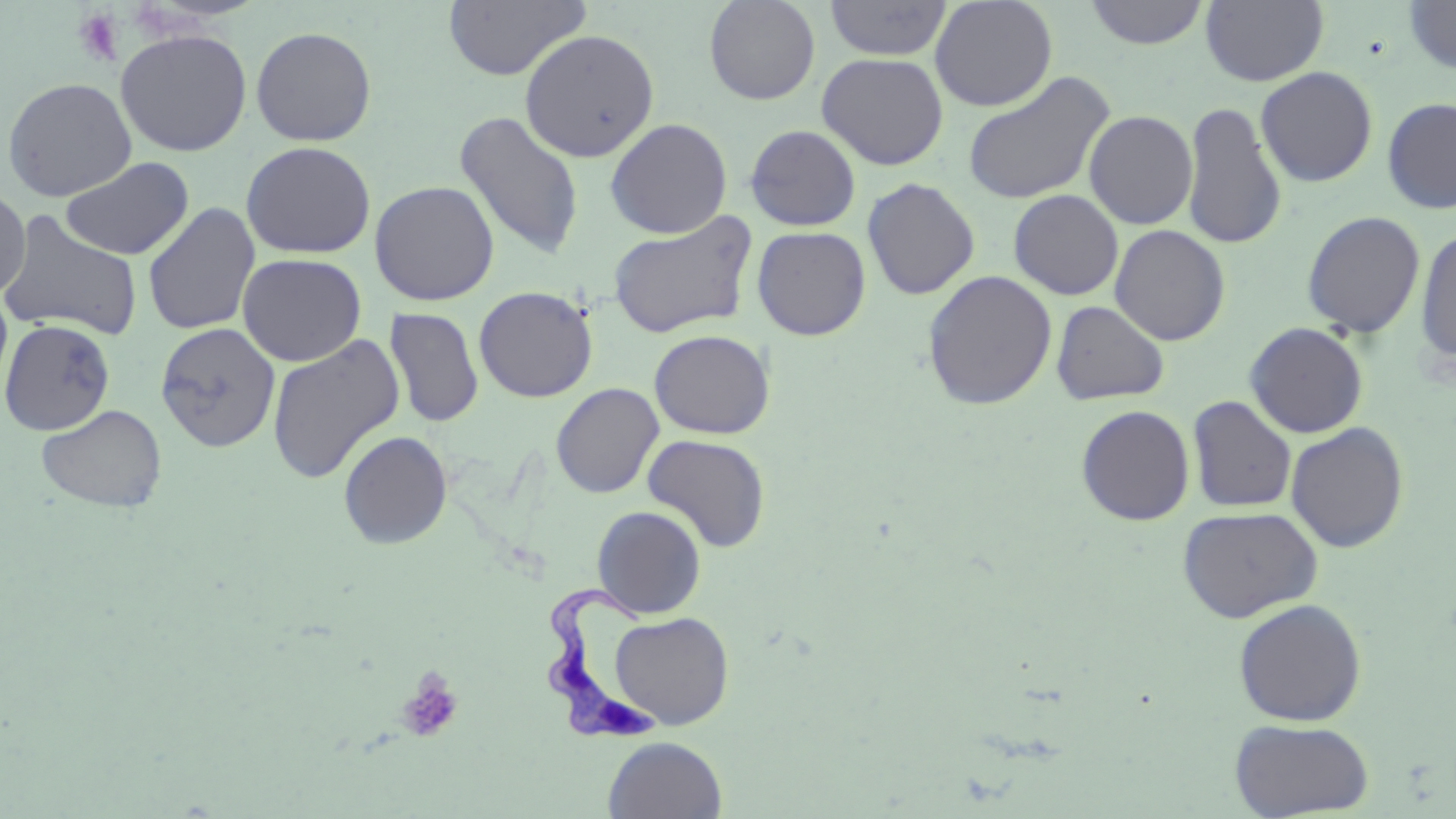
slide_level_diagnosis: Trypanosoma brucei
preparation: thin blood film
field_of_view: single
stain: May-Grünwald-Giemsa
uninfected_red_blood_cell_locations: 'approximate bounding boxes as (x1,y1)-(x2,y2) corner pairs in pixels: (703,0)-(821,105), (930,0)-(1058,111), (1084,0)-(1209,49), (443,1)-(591,81), (824,1)-(952,61), (1201,1)-(1329,86), (1402,1)-(1456,74), (250,25)-(377,146), (115,28)-(253,156), (519,28)-(660,162), (816,52)-(949,170), (1256,67)-(1378,187), (961,71)-(1115,206), (1,77)-(137,201), (1380,96)-(1456,214), (1181,101)-(1288,250), (454,110)-(585,260), (1083,110)-(1199,230), (605,118)-(733,239), (744,124)-(862,231), (240,141)-(376,259), (60,156)-(194,260), (862,177)-(980,301), (369,180)-(500,306), (0,186)-(30,300), (1008,189)-(1123,300), (142,202)-(260,336), (0,209)-(144,341), (1301,210)-(1426,338), (607,211)-(759,340), (1109,225)-(1231,346), (751,226)-(871,341), (1415,227)-(1456,367), (237,253)-(367,366), (922,270)-(1058,410), (473,285)-(598,402), (0,287)-(13,397), (1051,300)-(1169,405), (384,307)-(484,429), (1,318)-(115,435), (154,322)-(281,453), (1245,322)-(1369,438), (649,329)-(775,439), (267,334)-(405,484), (551,382)-(664,499), (1188,395)-(1298,513), (36,403)-(167,513), (1076,405)-(1195,526), (1285,422)-(1409,553), (338,430)-(453,549), (642,434)-(771,552), (591,505)-(707,618), (1177,506)-(1323,623), (1233,598)-(1367,727), (609,611)-(734,729), (1230,718)-(1374,818), (602,736)-(728,818)'
modality: optical microscopy
image_size: 1456×819 pixels
trypanosoma_brucei_locations: 'approximate bounding boxes as (x1,y1)-(x2,y2) corner pairs in pixels: (544,584)-(661,745)'
platelet_locations: 'approximate bounding boxes as (x1,y1)-(x2,y2) corner pairs in pixels: (72,8)-(127,67), (396,669)-(464,743)'
magnification: 1000x